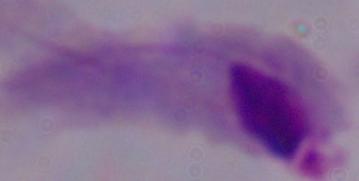
identification: trichomonad
magnification: 1000x
modality: photomicrograph